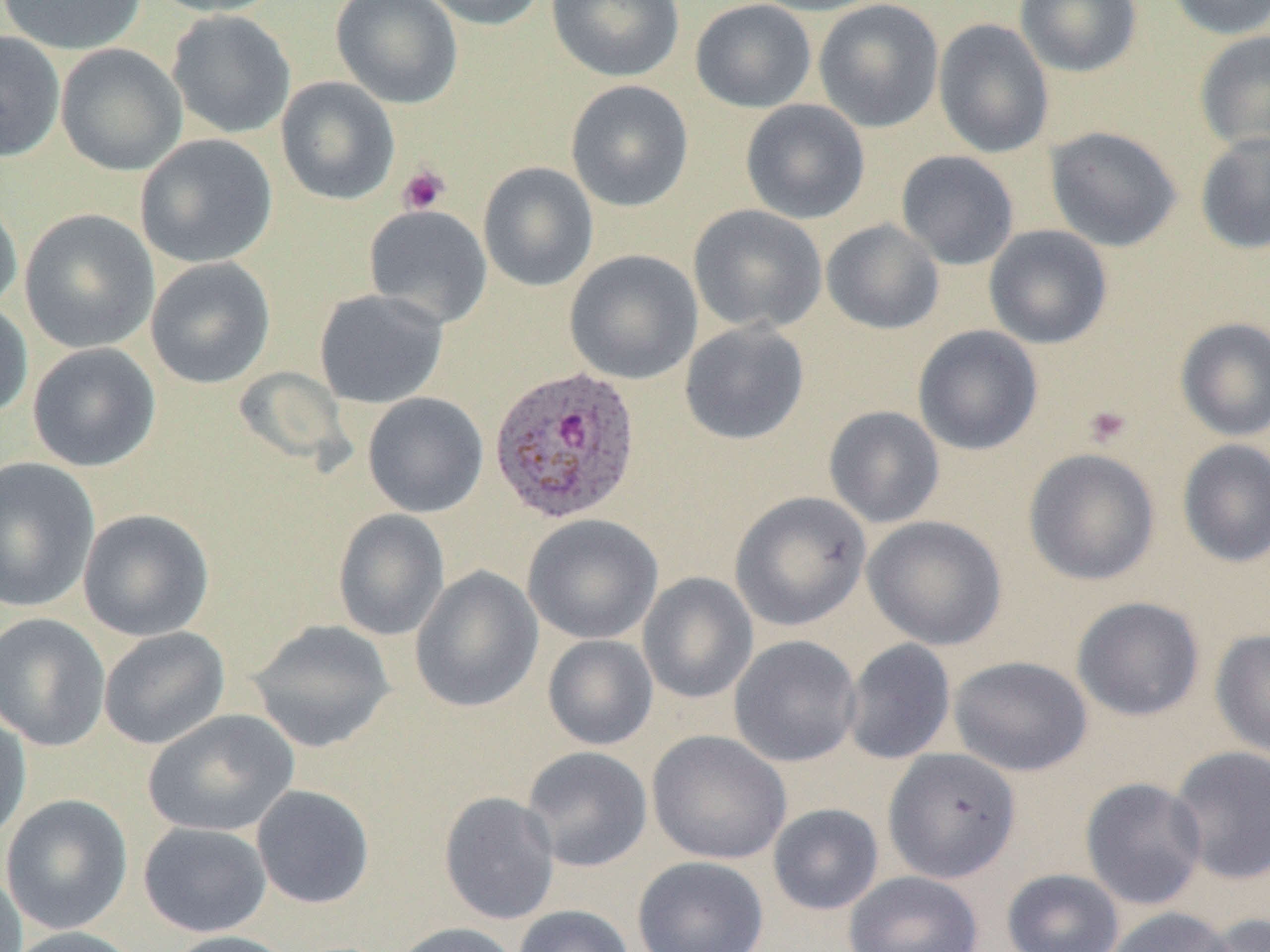

{
  "slide_level_diagnosis": "Plasmodium ovale",
  "field_of_view": "single",
  "magnification": "1000x",
  "uninfected_red_blood_cell_locations": "approximate bounding boxes as named x1/y1/x2/y2 corners in pixels: (x1=0, y1=0, x2=146, y2=55), (x1=147, y1=0, x2=284, y2=17), (x1=331, y1=0, x2=464, y2=109), (x1=417, y1=0, x2=548, y2=31), (x1=547, y1=0, x2=685, y2=82), (x1=690, y1=0, x2=817, y2=113), (x1=747, y1=0, x2=888, y2=16), (x1=813, y1=0, x2=944, y2=132), (x1=1014, y1=0, x2=1143, y2=77), (x1=1165, y1=0, x2=1270, y2=40), (x1=167, y1=10, x2=296, y2=139), (x1=933, y1=18, x2=1054, y2=158), (x1=0, y1=30, x2=65, y2=162), (x1=1194, y1=31, x2=1270, y2=154), (x1=55, y1=43, x2=187, y2=176), (x1=276, y1=76, x2=400, y2=205), (x1=565, y1=79, x2=694, y2=212), (x1=740, y1=99, x2=870, y2=224), (x1=1044, y1=125, x2=1182, y2=252), (x1=1194, y1=132, x2=1270, y2=255), (x1=135, y1=134, x2=278, y2=268), (x1=896, y1=150, x2=1019, y2=270), (x1=478, y1=162, x2=598, y2=291), (x1=0, y1=189, x2=22, y2=316), (x1=364, y1=204, x2=492, y2=328), (x1=688, y1=204, x2=827, y2=334), (x1=19, y1=209, x2=159, y2=353), (x1=821, y1=219, x2=944, y2=335), (x1=983, y1=224, x2=1113, y2=349), (x1=564, y1=249, x2=703, y2=385), (x1=145, y1=257, x2=276, y2=388), (x1=314, y1=288, x2=449, y2=408), (x1=0, y1=299, x2=33, y2=421), (x1=1175, y1=317, x2=1270, y2=442), (x1=679, y1=321, x2=810, y2=445), (x1=912, y1=325, x2=1043, y2=455), (x1=27, y1=342, x2=161, y2=472), (x1=362, y1=392, x2=488, y2=518), (x1=823, y1=405, x2=945, y2=528), (x1=1177, y1=439, x2=1270, y2=568), (x1=1023, y1=448, x2=1160, y2=586), (x1=0, y1=456, x2=100, y2=613), (x1=730, y1=491, x2=871, y2=631), (x1=78, y1=508, x2=215, y2=641), (x1=332, y1=509, x2=450, y2=641), (x1=523, y1=515, x2=663, y2=644), (x1=862, y1=515, x2=1007, y2=650), (x1=410, y1=565, x2=543, y2=713), (x1=638, y1=572, x2=758, y2=704), (x1=1071, y1=596, x2=1205, y2=721), (x1=0, y1=612, x2=110, y2=751), (x1=248, y1=619, x2=396, y2=753), (x1=98, y1=626, x2=231, y2=749), (x1=1211, y1=628, x2=1270, y2=760), (x1=542, y1=635, x2=658, y2=750), (x1=729, y1=635, x2=862, y2=767), (x1=842, y1=638, x2=956, y2=765), (x1=948, y1=655, x2=1093, y2=776), (x1=0, y1=708, x2=32, y2=846), (x1=143, y1=709, x2=300, y2=837), (x1=647, y1=730, x2=791, y2=865), (x1=521, y1=746, x2=653, y2=872), (x1=1167, y1=746, x2=1270, y2=885), (x1=883, y1=748, x2=1021, y2=883), (x1=1080, y1=777, x2=1208, y2=911), (x1=250, y1=784, x2=375, y2=909), (x1=439, y1=790, x2=560, y2=926), (x1=1, y1=794, x2=133, y2=935), (x1=767, y1=803, x2=884, y2=915), (x1=138, y1=821, x2=272, y2=937), (x1=632, y1=856, x2=769, y2=952), (x1=0, y1=866, x2=27, y2=952), (x1=1002, y1=868, x2=1124, y2=952), (x1=843, y1=871, x2=984, y2=952), (x1=512, y1=904, x2=636, y2=952), (x1=1104, y1=906, x2=1241, y2=952), (x1=1198, y1=913, x2=1270, y2=952), (x1=389, y1=921, x2=521, y2=952), (x1=6, y1=925, x2=142, y2=952), (x1=160, y1=930, x2=298, y2=952)",
  "platelet_locations": "approximate bounding boxes as named x1/y1/x2/y2 corners in pixels: (x1=397, y1=165, x2=450, y2=215), (x1=1082, y1=404, x2=1133, y2=448)",
  "preparation": "thin blood smear",
  "modality": "light microscopy",
  "plasmodium_ovale_infected_red_blood_cell_locations": "approximate bounding boxes as named x1/y1/x2/y2 corners in pixels: (x1=489, y1=364, x2=642, y2=525)",
  "image_size": "1270×952 pixels"
}